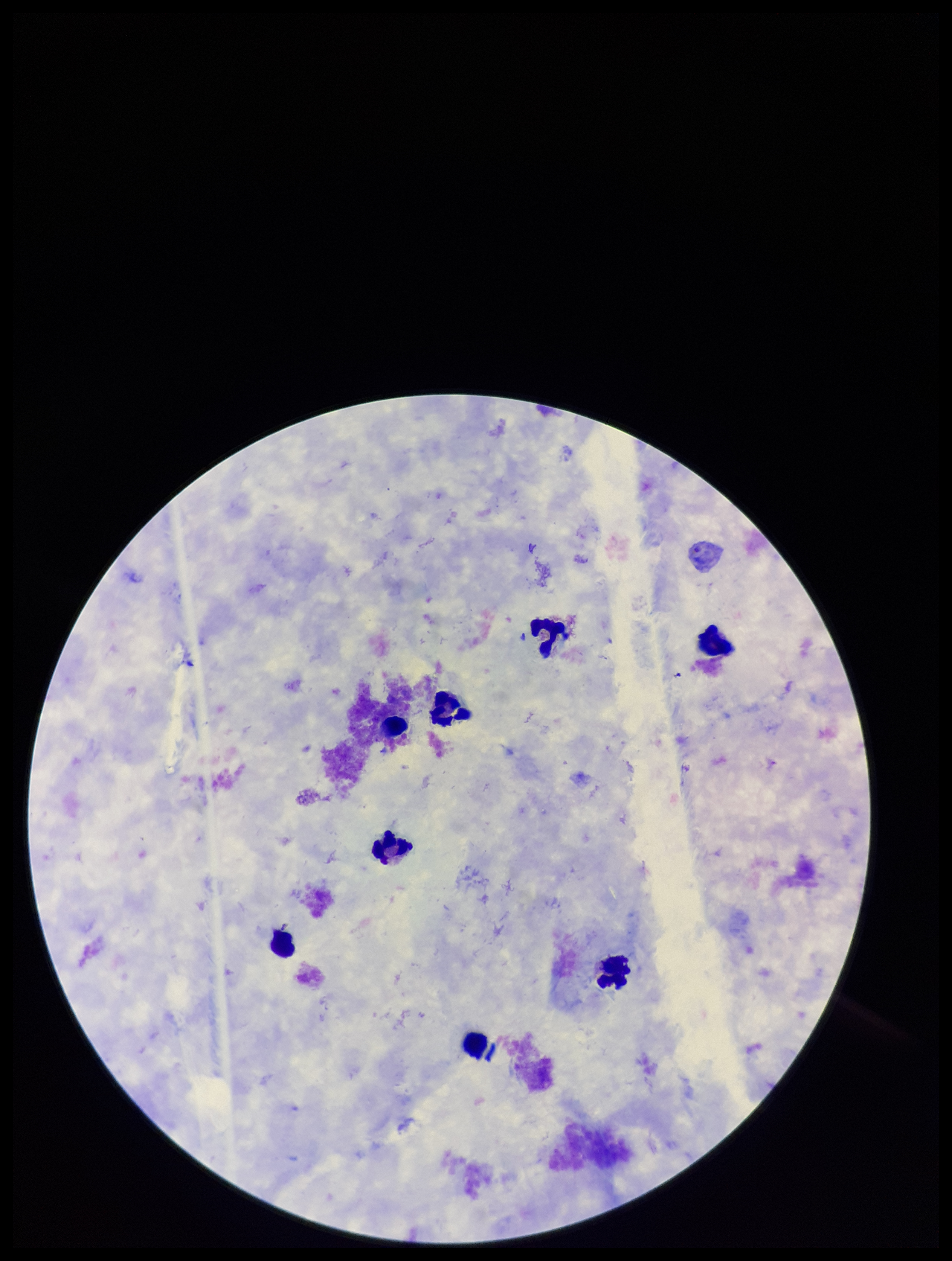
Summary:
  - Parasite count: 0
  - Capture: smartphone photograph through the microscope eyepiece
  - Preparation: thick smear
  - Image size: 952×1261 pixels
  - Plasmodium parasites: none seen
  - Stain: Giemsa
  - Field of view: single
  - Leukocyte count: 9
  - Patient malaria status: negative